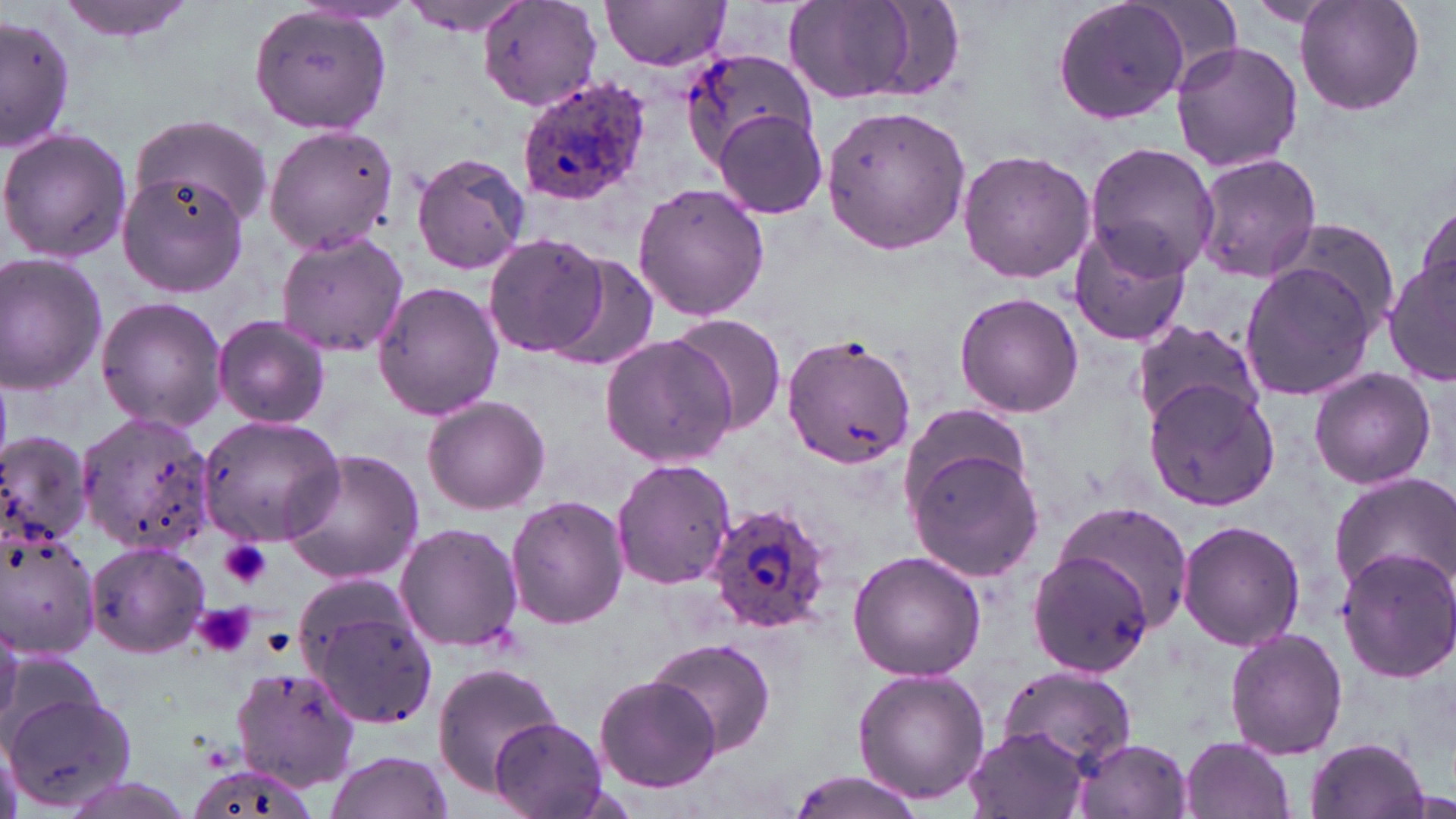
{
  "slide_level_diagnosis": "Plasmodium ovale",
  "uninfected_red_blood_cell_locations": "approximate bounding boxes as named x1/y1/x2/y2 corners in pixels: (x1=53, y1=0, x2=199, y2=44), (x1=395, y1=0, x2=529, y2=34), (x1=479, y1=0, x2=603, y2=113), (x1=602, y1=0, x2=733, y2=71), (x1=782, y1=0, x2=920, y2=104), (x1=1049, y1=0, x2=1196, y2=126), (x1=1293, y1=0, x2=1426, y2=118), (x1=247, y1=6, x2=394, y2=135), (x1=1, y1=15, x2=76, y2=152), (x1=1169, y1=40, x2=1303, y2=174), (x1=679, y1=45, x2=815, y2=170), (x1=822, y1=103, x2=971, y2=254), (x1=713, y1=107, x2=829, y2=221), (x1=131, y1=112, x2=273, y2=227), (x1=263, y1=124, x2=401, y2=254), (x1=0, y1=127, x2=132, y2=265), (x1=1084, y1=141, x2=1218, y2=279), (x1=957, y1=147, x2=1096, y2=285), (x1=410, y1=151, x2=531, y2=276), (x1=1193, y1=152, x2=1323, y2=283), (x1=117, y1=172, x2=250, y2=296), (x1=632, y1=182, x2=771, y2=323), (x1=1412, y1=202, x2=1454, y2=305), (x1=1274, y1=220, x2=1401, y2=332), (x1=1068, y1=225, x2=1194, y2=346), (x1=274, y1=230, x2=409, y2=358), (x1=481, y1=233, x2=608, y2=357), (x1=0, y1=252, x2=108, y2=395), (x1=548, y1=253, x2=660, y2=371), (x1=1383, y1=255, x2=1456, y2=388), (x1=1238, y1=260, x2=1378, y2=400), (x1=372, y1=280, x2=505, y2=420), (x1=955, y1=292, x2=1084, y2=418), (x1=96, y1=296, x2=228, y2=434), (x1=666, y1=314, x2=789, y2=437), (x1=212, y1=317, x2=330, y2=427), (x1=1129, y1=321, x2=1267, y2=430), (x1=780, y1=333, x2=916, y2=469), (x1=599, y1=334, x2=738, y2=467), (x1=1308, y1=367, x2=1436, y2=490), (x1=1142, y1=380, x2=1281, y2=512), (x1=421, y1=395, x2=551, y2=513), (x1=895, y1=408, x2=1035, y2=522), (x1=75, y1=409, x2=220, y2=557), (x1=197, y1=416, x2=345, y2=543), (x1=0, y1=431, x2=94, y2=553), (x1=908, y1=447, x2=1044, y2=581), (x1=282, y1=448, x2=423, y2=584), (x1=610, y1=458, x2=735, y2=592), (x1=1328, y1=474, x2=1456, y2=600), (x1=505, y1=496, x2=629, y2=630), (x1=1052, y1=502, x2=1195, y2=633), (x1=1178, y1=520, x2=1305, y2=652), (x1=394, y1=521, x2=524, y2=652), (x1=1, y1=529, x2=100, y2=661), (x1=85, y1=539, x2=211, y2=658), (x1=1332, y1=546, x2=1455, y2=681), (x1=847, y1=549, x2=988, y2=681), (x1=1026, y1=549, x2=1155, y2=677), (x1=300, y1=587, x2=440, y2=731), (x1=0, y1=616, x2=23, y2=737), (x1=1224, y1=627, x2=1349, y2=760), (x1=648, y1=638, x2=775, y2=757), (x1=432, y1=664, x2=563, y2=793), (x1=231, y1=666, x2=363, y2=791), (x1=995, y1=666, x2=1137, y2=773), (x1=853, y1=668, x2=990, y2=804), (x1=1, y1=669, x2=128, y2=804), (x1=593, y1=673, x2=722, y2=792), (x1=490, y1=717, x2=607, y2=818), (x1=963, y1=723, x2=1092, y2=819), (x1=1179, y1=736, x2=1296, y2=819), (x1=1303, y1=736, x2=1431, y2=819), (x1=1071, y1=738, x2=1192, y2=819), (x1=323, y1=750, x2=452, y2=819), (x1=184, y1=759, x2=316, y2=819), (x1=785, y1=771, x2=927, y2=819)",
  "plasmodium_ovale_infected_red_blood_cell_locations": "approximate bounding boxes as named x1/y1/x2/y2 corners in pixels: (x1=515, y1=76, x2=653, y2=205), (x1=703, y1=502, x2=834, y2=636)",
  "stain": "May-Grünwald-Giemsa",
  "modality": "optical microscopy",
  "preparation": "thin blood smear",
  "platelet_locations": "approximate bounding boxes as named x1/y1/x2/y2 corners in pixels: (x1=217, y1=537, x2=272, y2=588), (x1=220, y1=540, x2=271, y2=590), (x1=195, y1=601, x2=254, y2=656), (x1=193, y1=605, x2=254, y2=659)",
  "magnification": "1000x",
  "field_of_view": "one of a larger specimen",
  "image_size": "1456×819 pixels"
}